Assess the morphology of the erythrocytes.
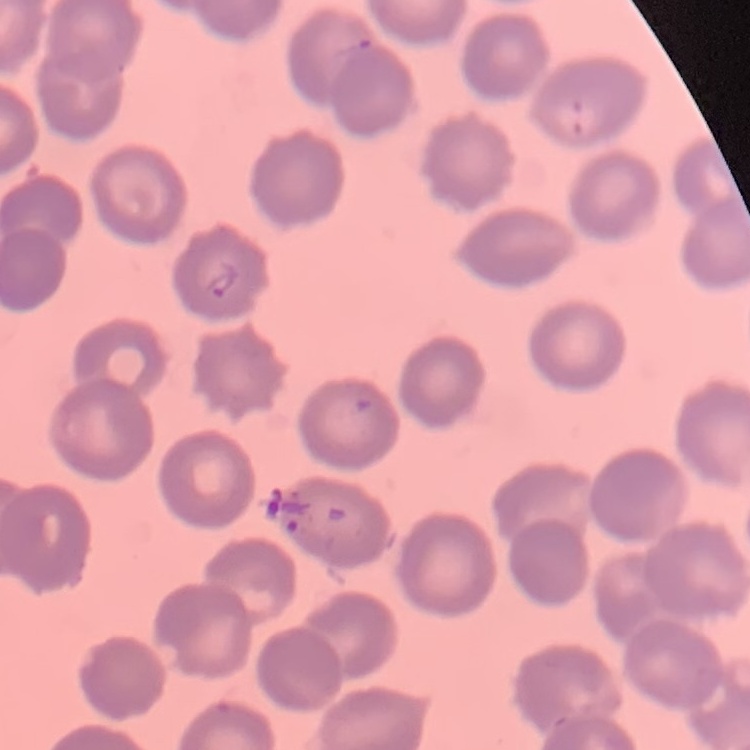

They show no rouleaux formation.

Summary:
  - Preparation: thin peripheral smear
  - Stain: Field's or Giemsa
  - Image type: one tile cut from a larger photomicrograph